Report the malaria status of this cell.
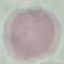

Uninfected.

preparation: thin blood film
stain: Giemsa
capture: smartphone through the microscope eyepiece
image_type: cell patch, automatically extracted from a larger field of view and resized to 64 × 64 pixels